Report the malaria status of this cell.
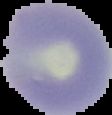

Uninfected.

Summary:
  - Preparation: thin blood film
  - Image size: 112×115 pixels
  - Image type: cell region segmented out of the field of view; surrounding area masked to black